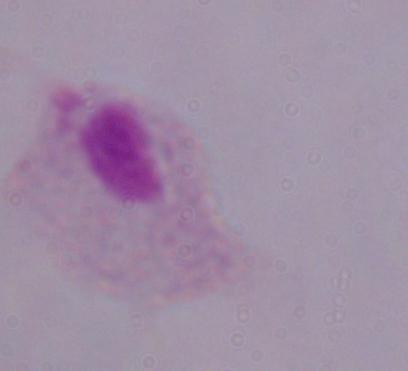

{
  "magnification": "1000x",
  "identification": "trichomonad",
  "modality": "photomicrograph"
}